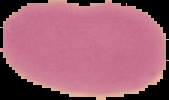

{
  "preparation": "thin blood smear",
  "result": "no malaria parasites seen",
  "image_type": "segmented cell region on a black background",
  "image_size": "169×100 pixels"
}